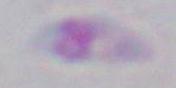
modality = photomicrograph
identification = Toxoplasma gondii
magnification = 1000x